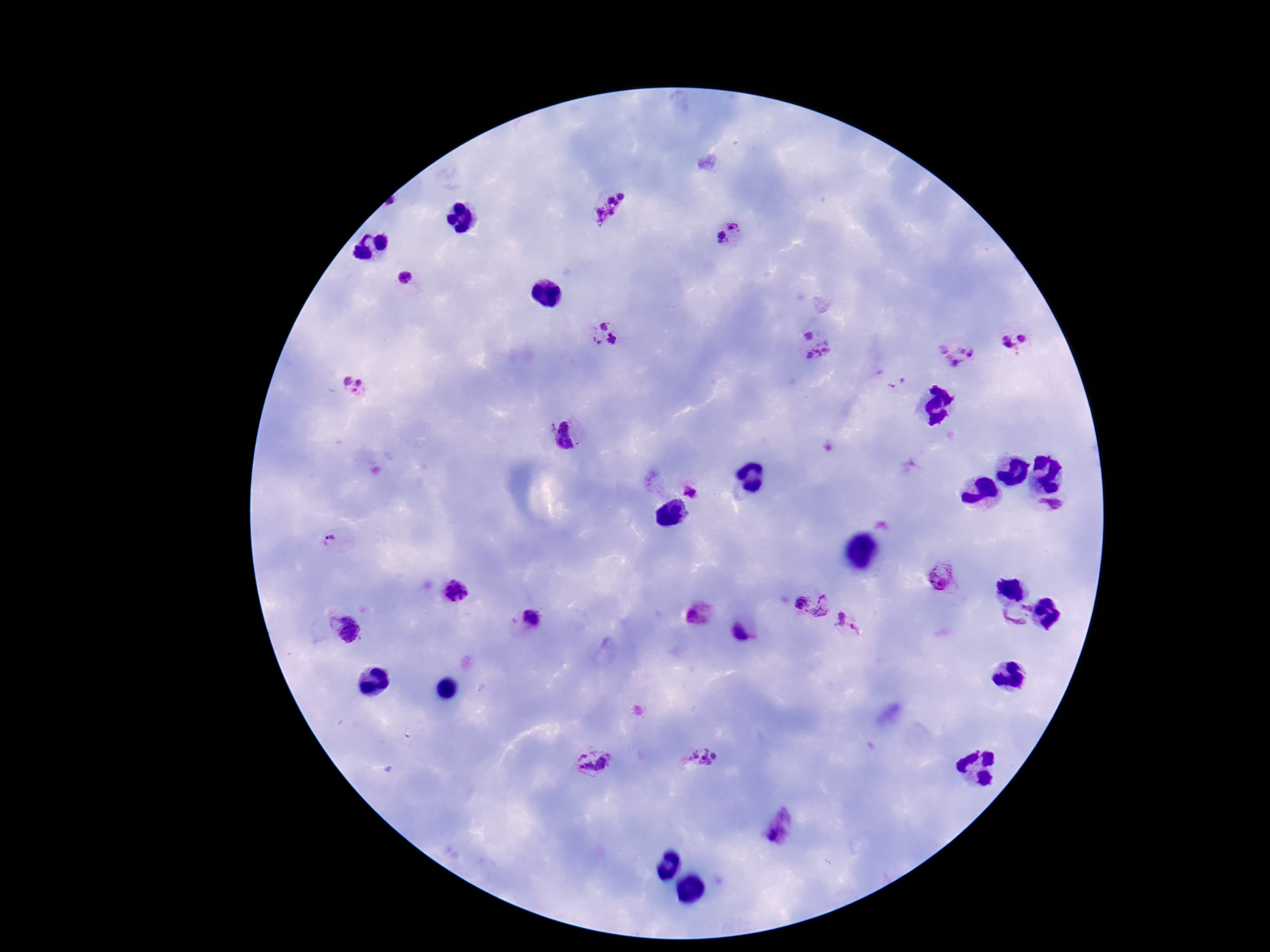
Approximate centers as {x, y} in pixels.
Summary:
  - Plasmodium parasite locations: {611, 207}, {735, 221}, {721, 240}, {405, 277}, {603, 323}, {809, 334}, {1018, 337}, {612, 339}, {596, 344}, {958, 354}, {824, 356}, {898, 382}, {351, 386}, {570, 436}, {690, 490}, {1053, 507}, {339, 535}, {940, 575}, {455, 594}, {801, 604}, {827, 608}, {1019, 614}, {700, 615}, {532, 621}, {849, 626}, {344, 630}, {745, 633}, {701, 757}, {594, 759}, {781, 826}
  - Image size: 1270×952 pixels
  - Preparation: thick blood smear
  - Capture: smartphone camera through the microscope eyepiece
  - Stain: Giemsa
  - Field of view: one from this slide
  - Patient malaria status: infected
  - Magnification: 100x